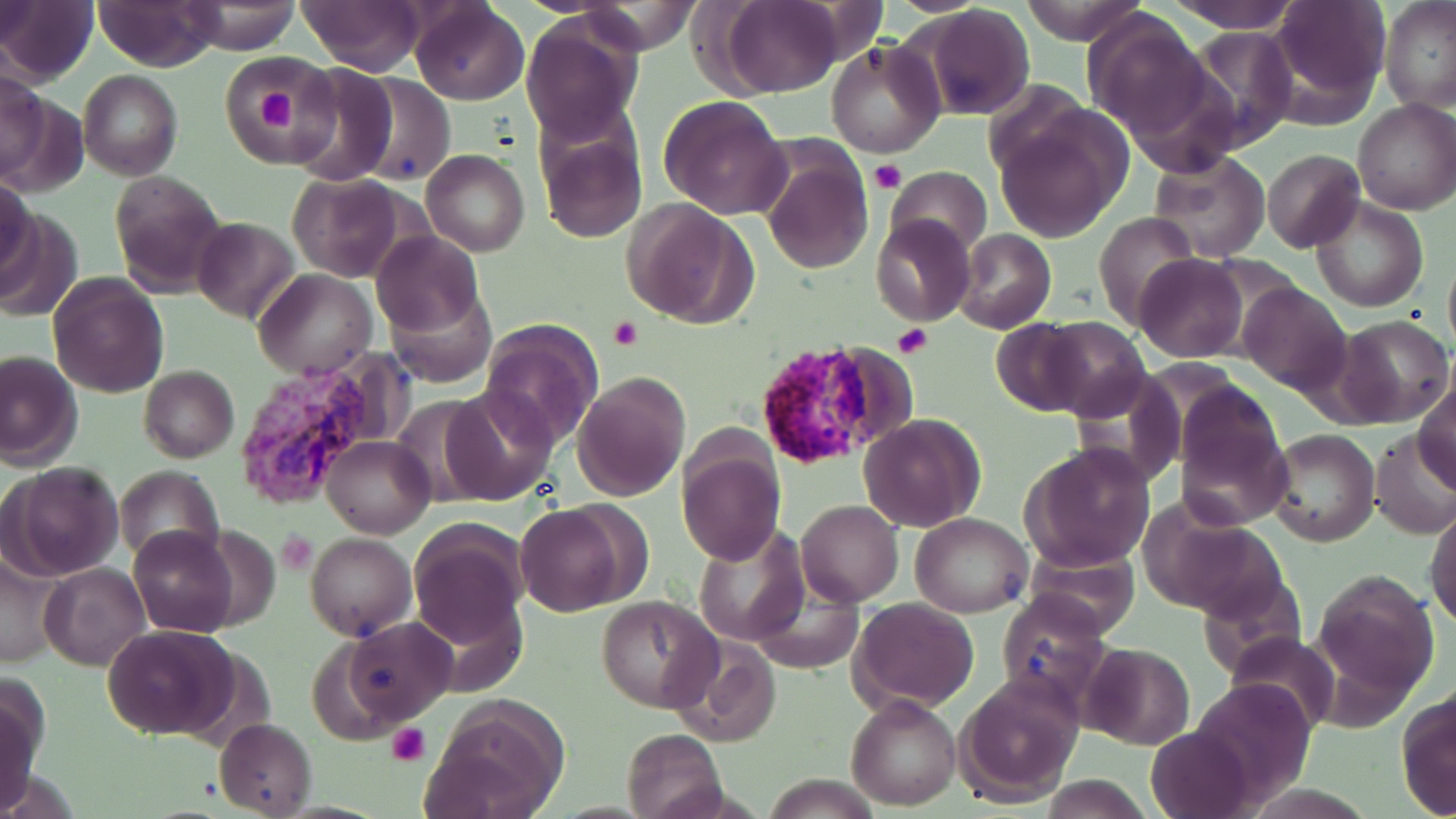
Approximate bounding boxes as [x1, y1, x2, y2] in pixels. Plasmodium vivax-infected red blood cell locations: [229, 351, 410, 513]. Uninfected red blood cell locations: [0, 0, 97, 87], [93, 0, 224, 71], [182, 0, 301, 54], [296, 0, 427, 76], [410, 0, 528, 107], [719, 0, 845, 97], [1018, 0, 1148, 45], [1165, 0, 1299, 33], [1267, 0, 1390, 121], [1380, 2, 1456, 114], [911, 6, 1037, 121], [1082, 10, 1214, 139], [522, 14, 644, 147], [1180, 29, 1299, 155], [825, 37, 945, 157], [214, 53, 336, 162], [281, 64, 405, 185], [0, 67, 47, 183], [79, 70, 183, 181], [354, 72, 454, 186], [982, 80, 1089, 182], [659, 94, 791, 221], [1353, 99, 1456, 217], [999, 109, 1131, 241], [535, 114, 649, 245], [757, 138, 874, 276], [1147, 148, 1271, 261], [1262, 148, 1366, 254], [423, 150, 530, 257], [887, 166, 993, 256], [108, 171, 228, 297], [288, 173, 407, 281], [0, 176, 35, 280], [1311, 196, 1429, 312], [623, 200, 758, 331], [0, 208, 83, 322], [1094, 212, 1202, 331], [870, 215, 975, 326], [191, 217, 299, 322], [371, 229, 486, 336], [954, 230, 1056, 334], [1135, 254, 1248, 362], [1442, 254, 1456, 357], [253, 267, 376, 379], [48, 272, 169, 397], [1238, 282, 1353, 396], [388, 288, 497, 389], [1336, 314, 1456, 428], [1034, 317, 1152, 422], [990, 318, 1103, 418], [478, 320, 601, 447], [822, 346, 922, 447], [0, 352, 84, 473], [139, 365, 239, 463], [1066, 369, 1188, 492], [571, 373, 689, 502], [1416, 377, 1456, 491], [1172, 380, 1293, 525], [442, 385, 557, 505], [858, 414, 984, 531], [1371, 428, 1456, 542], [1268, 429, 1378, 546], [322, 435, 435, 538], [678, 440, 785, 564], [315, 443, 425, 660], [1019, 443, 1155, 572], [5, 461, 126, 582], [113, 466, 225, 568], [797, 500, 905, 607], [516, 502, 633, 617], [1425, 502, 1456, 629], [1141, 510, 1288, 622], [909, 512, 1032, 618], [407, 519, 529, 645], [692, 524, 810, 646], [127, 526, 238, 636], [277, 529, 317, 573], [304, 533, 417, 642], [1024, 546, 1143, 638], [1, 548, 63, 672], [41, 562, 150, 671], [1310, 570, 1441, 702], [748, 585, 863, 673], [996, 591, 1112, 709], [598, 596, 720, 713], [850, 598, 980, 710], [339, 617, 457, 727], [102, 623, 239, 740], [1224, 632, 1342, 734], [667, 638, 782, 747], [1081, 643, 1196, 749], [954, 675, 1083, 805], [1187, 677, 1317, 807], [1, 680, 44, 813], [1396, 688, 1456, 819], [847, 693, 962, 809], [423, 697, 568, 819], [215, 718, 318, 816], [1148, 724, 1253, 819], [622, 728, 728, 819], [762, 774, 884, 817], [1038, 776, 1153, 818]. Platelet locations: [253, 84, 299, 138], [870, 160, 904, 194], [609, 315, 640, 350], [893, 326, 930, 357], [277, 530, 315, 573], [388, 724, 431, 767]. Slide-level diagnosis: Plasmodium vivax. 1000x magnification. May-Grünwald-Giemsa stain. Thin blood smear. One field of a larger specimen. Light microscopy. Image is 1456×819 pixels.